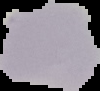
Summary:
  - Image type: cell region segmented out of the field of view; surrounding area masked to black
  - Image size: 100×91 pixels
  - Preparation: thin blood smear
  - Result: negative for Plasmodium parasites